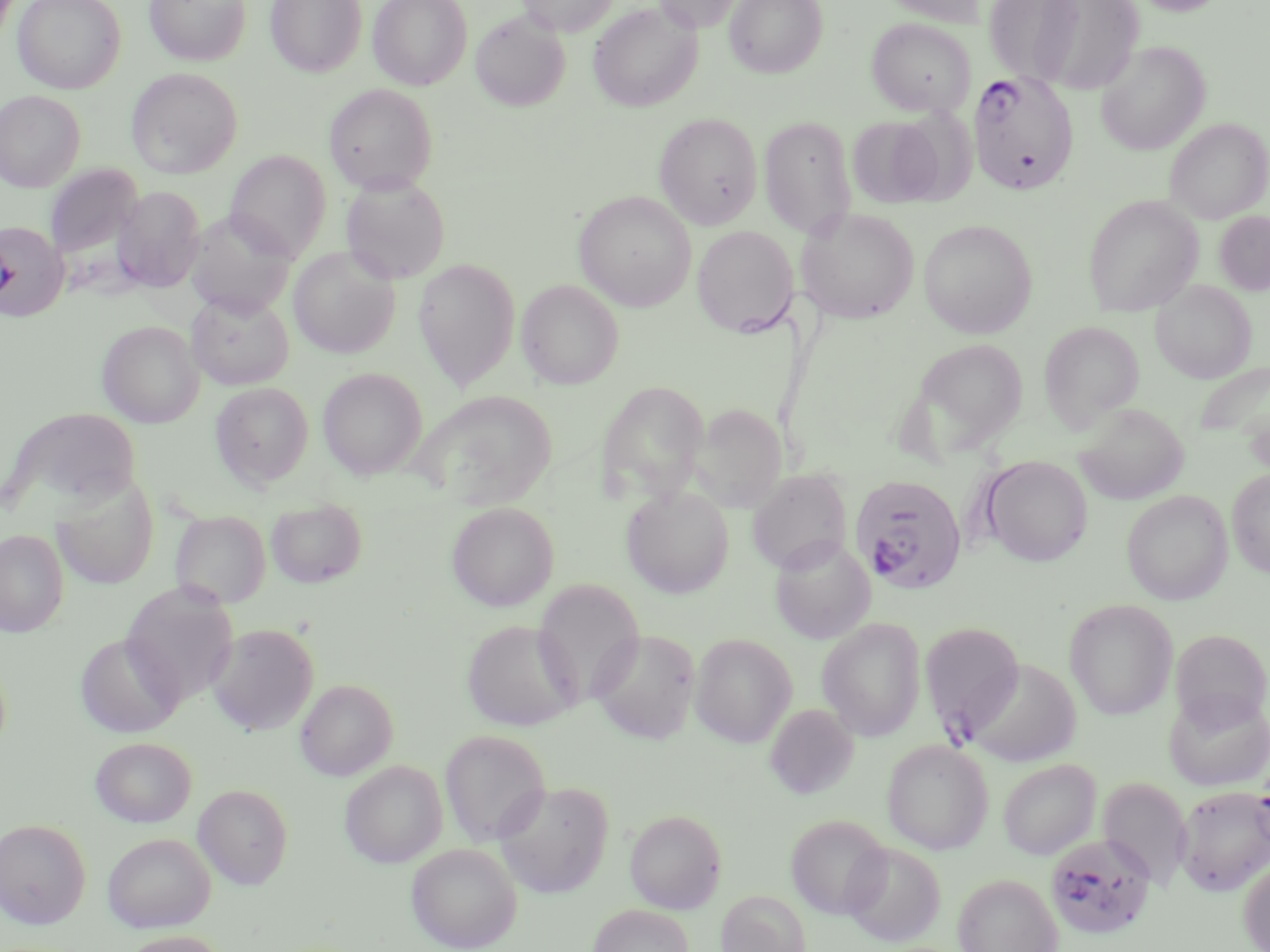 Approximate bounding boxes as named x1/y1/x2/y2 corners in pixels. Uninfected red blood cell locations: (x1=13, y1=0, x2=125, y2=94), (x1=144, y1=0, x2=252, y2=66), (x1=266, y1=0, x2=366, y2=77), (x1=368, y1=0, x2=472, y2=89), (x1=517, y1=0, x2=619, y2=36), (x1=652, y1=0, x2=744, y2=32), (x1=724, y1=0, x2=828, y2=78), (x1=878, y1=0, x2=985, y2=27), (x1=983, y1=0, x2=1086, y2=85), (x1=1022, y1=0, x2=1146, y2=95), (x1=1129, y1=0, x2=1228, y2=15), (x1=588, y1=2, x2=702, y2=112), (x1=470, y1=10, x2=570, y2=112), (x1=866, y1=17, x2=976, y2=117), (x1=1096, y1=40, x2=1210, y2=155), (x1=126, y1=68, x2=242, y2=178), (x1=324, y1=84, x2=438, y2=194), (x1=0, y1=90, x2=85, y2=192), (x1=654, y1=112, x2=763, y2=230), (x1=759, y1=116, x2=857, y2=239), (x1=847, y1=116, x2=945, y2=208), (x1=1165, y1=118, x2=1269, y2=223), (x1=225, y1=150, x2=331, y2=259), (x1=45, y1=164, x2=144, y2=263), (x1=341, y1=175, x2=450, y2=284), (x1=112, y1=186, x2=206, y2=293), (x1=574, y1=191, x2=696, y2=311), (x1=1082, y1=195, x2=1203, y2=317), (x1=796, y1=208, x2=919, y2=324), (x1=185, y1=211, x2=298, y2=317), (x1=1214, y1=211, x2=1270, y2=296), (x1=919, y1=219, x2=1037, y2=338), (x1=0, y1=221, x2=69, y2=321), (x1=692, y1=226, x2=798, y2=336), (x1=288, y1=247, x2=400, y2=358), (x1=413, y1=258, x2=520, y2=390), (x1=517, y1=279, x2=623, y2=389), (x1=1151, y1=280, x2=1256, y2=383), (x1=186, y1=291, x2=294, y2=389), (x1=97, y1=321, x2=204, y2=428), (x1=1038, y1=321, x2=1144, y2=431), (x1=907, y1=338, x2=1031, y2=458), (x1=1194, y1=359, x2=1270, y2=444), (x1=318, y1=367, x2=427, y2=479), (x1=596, y1=380, x2=709, y2=503), (x1=210, y1=382, x2=314, y2=490), (x1=414, y1=390, x2=558, y2=509), (x1=692, y1=403, x2=787, y2=512), (x1=1073, y1=403, x2=1188, y2=505), (x1=4, y1=407, x2=141, y2=518), (x1=980, y1=455, x2=1093, y2=566), (x1=747, y1=469, x2=852, y2=574), (x1=1227, y1=469, x2=1270, y2=577), (x1=51, y1=479, x2=159, y2=590), (x1=621, y1=485, x2=734, y2=598), (x1=1121, y1=491, x2=1232, y2=604), (x1=265, y1=498, x2=367, y2=588), (x1=446, y1=501, x2=559, y2=611), (x1=171, y1=510, x2=271, y2=609), (x1=0, y1=529, x2=68, y2=637), (x1=769, y1=535, x2=876, y2=644), (x1=532, y1=578, x2=645, y2=708), (x1=120, y1=583, x2=239, y2=706), (x1=1065, y1=600, x2=1178, y2=720), (x1=817, y1=617, x2=926, y2=741), (x1=461, y1=619, x2=581, y2=731), (x1=919, y1=622, x2=1026, y2=735), (x1=207, y1=623, x2=319, y2=735), (x1=591, y1=628, x2=701, y2=744), (x1=1169, y1=628, x2=1270, y2=729), (x1=74, y1=632, x2=185, y2=738), (x1=690, y1=632, x2=797, y2=747), (x1=963, y1=658, x2=1081, y2=766), (x1=296, y1=679, x2=397, y2=781), (x1=1164, y1=690, x2=1270, y2=791), (x1=765, y1=704, x2=859, y2=799), (x1=440, y1=729, x2=551, y2=847), (x1=90, y1=736, x2=196, y2=827), (x1=881, y1=739, x2=993, y2=854), (x1=998, y1=759, x2=1100, y2=860), (x1=340, y1=760, x2=447, y2=868), (x1=1098, y1=776, x2=1192, y2=889), (x1=493, y1=780, x2=613, y2=898), (x1=193, y1=783, x2=294, y2=889), (x1=1176, y1=785, x2=1270, y2=896), (x1=625, y1=809, x2=727, y2=913), (x1=785, y1=814, x2=891, y2=919), (x1=0, y1=819, x2=91, y2=928), (x1=102, y1=832, x2=216, y2=932), (x1=842, y1=841, x2=946, y2=947), (x1=406, y1=843, x2=522, y2=951), (x1=1238, y1=857, x2=1270, y2=952), (x1=953, y1=873, x2=1062, y2=952), (x1=716, y1=889, x2=810, y2=952), (x1=588, y1=904, x2=694, y2=952), (x1=117, y1=930, x2=231, y2=952). Plasmodium falciparum-infected red blood cell locations: (x1=969, y1=70, x2=1078, y2=195), (x1=850, y1=473, x2=968, y2=595), (x1=1044, y1=832, x2=1157, y2=940). Slide-level diagnosis: Plasmodium falciparum. Thin blood smear. Optical microscopy. May-Grünwald-Giemsa stain. Single field of view. Captured at 1000x magnification. Image is 1270×952 pixels.